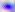
modality = photomicrograph
magnification = 400x
identification = Toxoplasma gondii